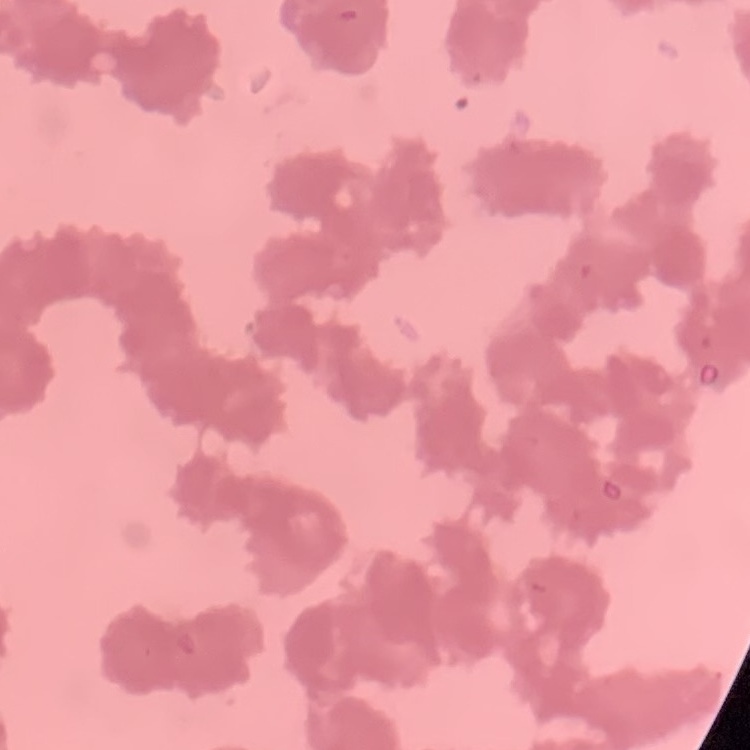

erythrocyte_morphology: rouleaux formation
stain: Field's or Giemsa
image_type: one tile cut from a larger photomicrograph
preparation: thin peripheral smear